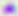
modality = photomicrograph
magnification = 400x
identification = Toxoplasma gondii